Outline each blood parasite and name the species.
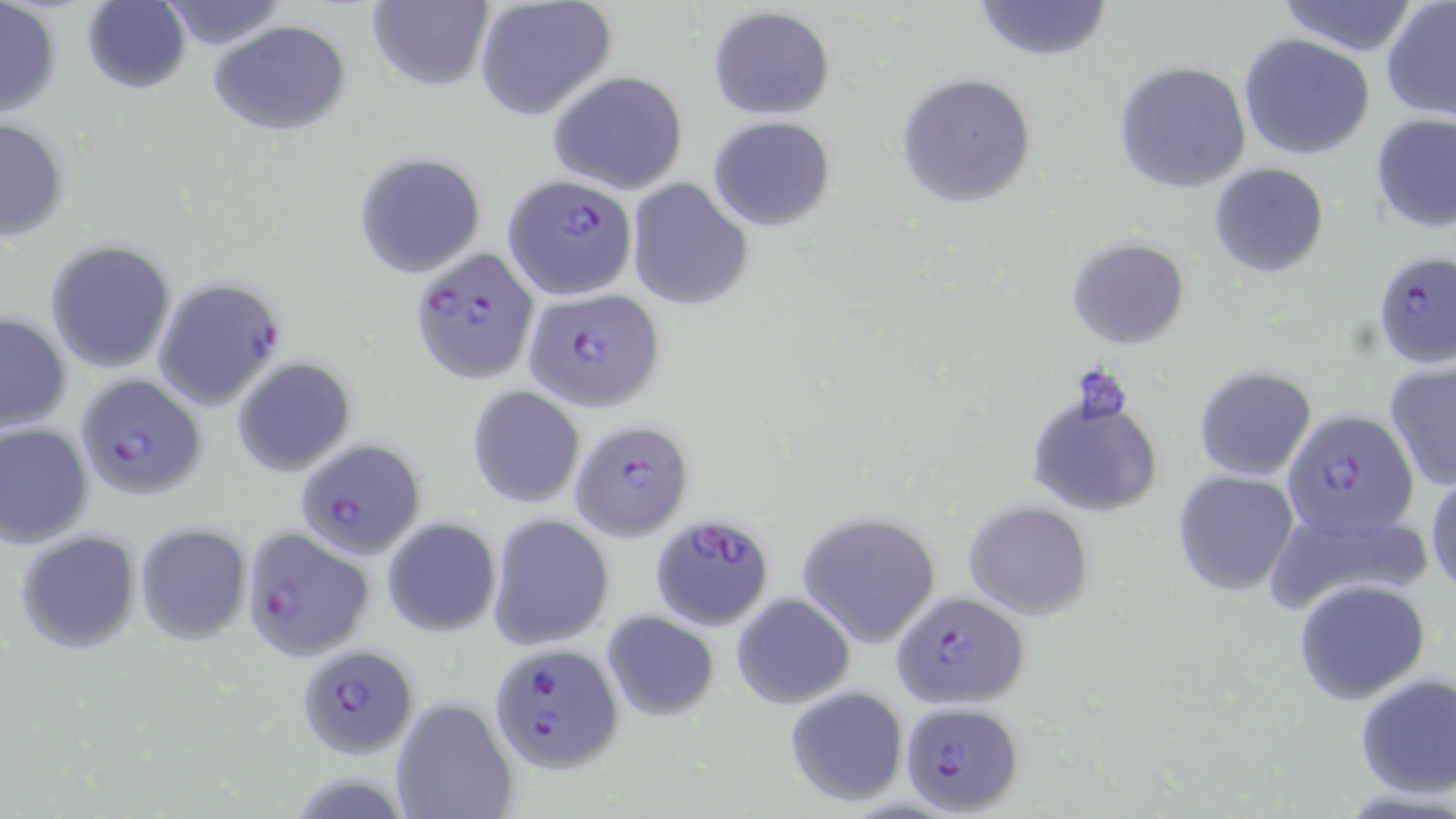
Approximate bounding boxes as named x1/y1/x2/y2 corners in pixels.
Plasmodium falciparum-infected red blood cells: (x1=504, y1=172, x2=636, y2=300), (x1=412, y1=246, x2=540, y2=383), (x1=1375, y1=252, x2=1453, y2=373), (x1=153, y1=277, x2=285, y2=410), (x1=523, y1=288, x2=663, y2=412), (x1=78, y1=373, x2=205, y2=500), (x1=1284, y1=409, x2=1419, y2=539), (x1=570, y1=419, x2=695, y2=539), (x1=293, y1=437, x2=425, y2=561), (x1=650, y1=508, x2=774, y2=632), (x1=241, y1=527, x2=373, y2=661), (x1=891, y1=592, x2=1028, y2=711), (x1=295, y1=643, x2=419, y2=756), (x1=488, y1=644, x2=623, y2=773), (x1=900, y1=702, x2=1024, y2=814).
No Plasmodium ovale, Plasmodium malariae, Plasmodium vivax, Babesia divergens, or Trypanosoma brucei observed.

Uninfected red blood cell locations: (x1=0, y1=0, x2=62, y2=121), (x1=972, y1=0, x2=1115, y2=62), (x1=1277, y1=0, x2=1420, y2=57), (x1=82, y1=1, x2=191, y2=94), (x1=156, y1=1, x2=288, y2=51), (x1=366, y1=1, x2=491, y2=91), (x1=1381, y1=1, x2=1456, y2=121), (x1=473, y1=2, x2=618, y2=120), (x1=707, y1=7, x2=836, y2=118), (x1=209, y1=20, x2=352, y2=137), (x1=1238, y1=34, x2=1375, y2=159), (x1=1113, y1=60, x2=1252, y2=196), (x1=547, y1=71, x2=689, y2=195), (x1=895, y1=72, x2=1039, y2=209), (x1=1371, y1=114, x2=1455, y2=235), (x1=706, y1=117, x2=837, y2=230), (x1=0, y1=118, x2=71, y2=241), (x1=354, y1=152, x2=486, y2=278), (x1=1208, y1=162, x2=1330, y2=278), (x1=627, y1=179, x2=753, y2=310), (x1=1065, y1=237, x2=1189, y2=351), (x1=46, y1=241, x2=176, y2=372), (x1=0, y1=310, x2=72, y2=432), (x1=231, y1=356, x2=357, y2=477), (x1=1384, y1=362, x2=1456, y2=491), (x1=1194, y1=365, x2=1317, y2=481), (x1=467, y1=385, x2=585, y2=510), (x1=1027, y1=389, x2=1163, y2=520), (x1=0, y1=421, x2=94, y2=548), (x1=1425, y1=465, x2=1456, y2=597), (x1=1172, y1=470, x2=1299, y2=596), (x1=964, y1=501, x2=1093, y2=620), (x1=795, y1=511, x2=941, y2=649), (x1=488, y1=513, x2=614, y2=651), (x1=381, y1=515, x2=500, y2=638), (x1=134, y1=521, x2=253, y2=645), (x1=15, y1=529, x2=141, y2=654), (x1=1292, y1=577, x2=1431, y2=704), (x1=731, y1=594, x2=853, y2=709), (x1=601, y1=609, x2=719, y2=721), (x1=1354, y1=672, x2=1456, y2=799), (x1=784, y1=685, x2=910, y2=808), (x1=391, y1=697, x2=518, y2=819). Slide-level diagnosis: Plasmodium falciparum. May-Grünwald-Giemsa-stained preparation. One field of a larger specimen. Light microscopy. Thin blood smear. 1000x magnification. Image is 1456×819 pixels.